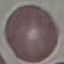

Summary:
  - Result: no malaria parasites seen
  - Stain: Giemsa
  - Preparation: thin smear
  - Capture: smartphone through the microscope eyepiece
  - Image type: cell patch, automatically extracted from a larger field of view and resized to 64 × 64 pixels